Identify the preparation type.
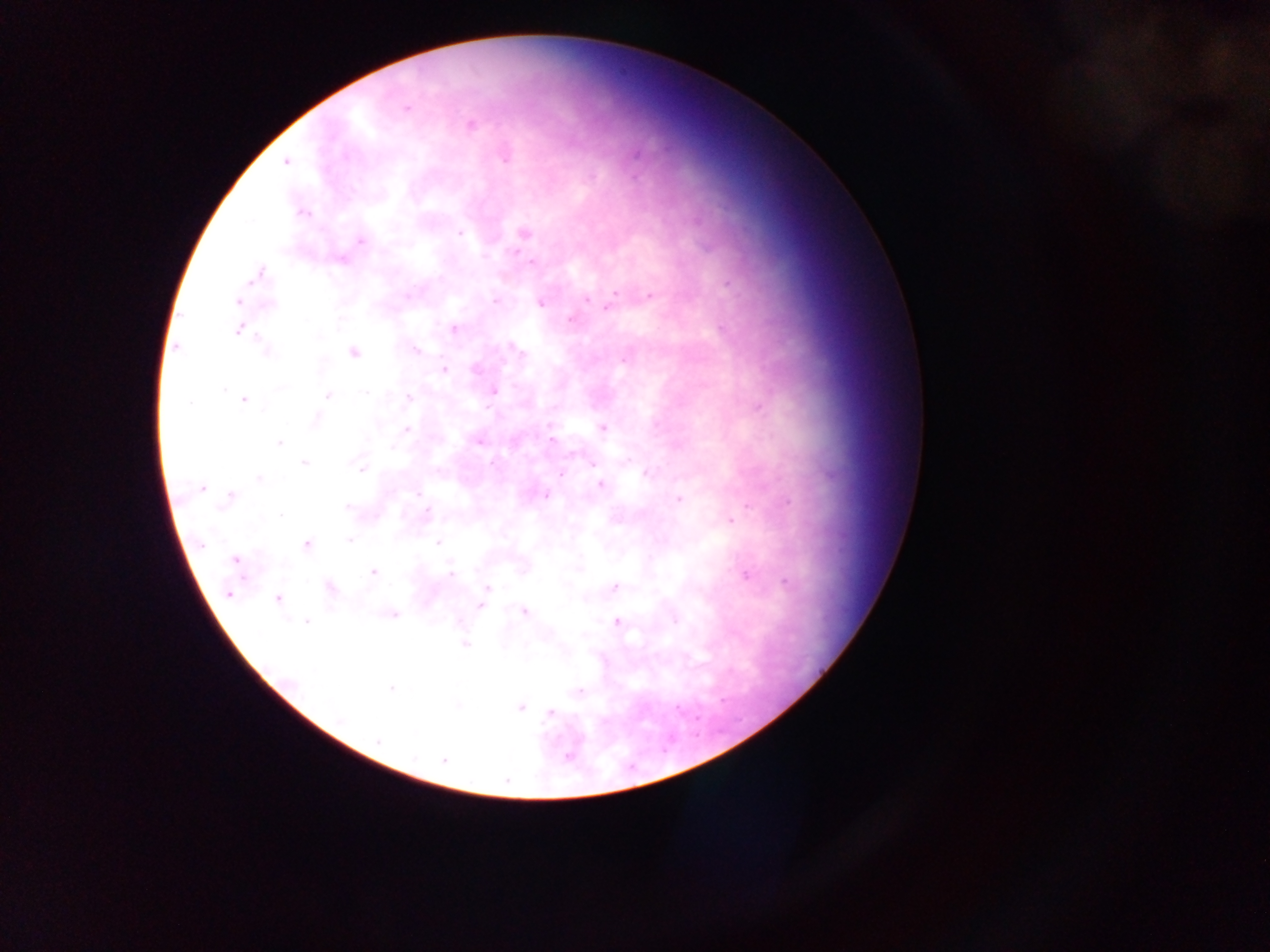

This is a thick smear.

Approximate centers as (x, y) in pixels. Plasmodium parasite locations: (406, 108), (471, 126), (636, 154), (504, 158), (287, 162), (635, 177), (302, 213), (525, 232), (459, 233), (361, 241), (517, 251), (526, 257), (340, 260), (531, 262), (260, 274), (727, 283), (616, 292), (651, 295), (585, 300), (238, 301), (495, 301), (540, 303), (271, 304), (608, 307), (571, 319), (341, 320), (454, 329), (238, 330), (320, 336), (177, 348), (516, 349), (267, 350), (415, 350), (353, 353), (522, 353), (625, 359), (475, 369), (445, 370), (280, 388), (224, 389), (494, 391), (365, 393), (328, 396), (409, 398), (245, 400), (758, 406), (488, 408), (317, 419), (602, 428), (407, 430), (551, 440), (279, 443), (479, 443), (573, 453), (305, 463), (492, 463), (592, 463), (361, 469), (561, 474), (646, 474), (260, 478), (600, 484), (202, 488), (418, 494), (231, 496), (545, 496), (679, 499), (788, 501), (228, 502), (347, 507), (746, 507), (427, 512), (280, 515), (730, 521), (350, 540), (438, 542), (201, 543), (306, 545), (235, 559), (373, 572), (451, 575), (746, 575), (785, 581), (614, 587), (331, 588), (487, 589), (229, 594), (278, 599), (480, 605), (524, 611), (394, 615), (675, 620), (306, 621), (616, 621), (464, 644), (391, 689), (579, 692), (520, 707), (550, 712), (341, 720), (378, 740), (566, 757), (444, 760). Mobile-phone photograph taken through the microscope. Image is 1270×952 pixels. Collected in Ghana. One field of view.